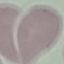
Summary:
  - Result: no malaria parasites detected
  - Capture: smartphone camera at the microscope eyepiece
  - Stain: Giemsa
  - Preparation: thin smear
  - Image type: automatically extracted cell patch, resized to 64 × 64 pixels